Classify this cell by malaria status.
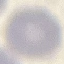

Uninfected.

preparation = thin smear
capture = smartphone through the microscope eyepiece
image type = automatically extracted cell patch, resized to 64 × 64 pixels
stain = Giemsa